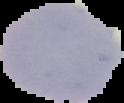

Result: negative for malaria parasites. Segmented cell region on a black background. Image is 124×103 pixels. From a thin blood smear.